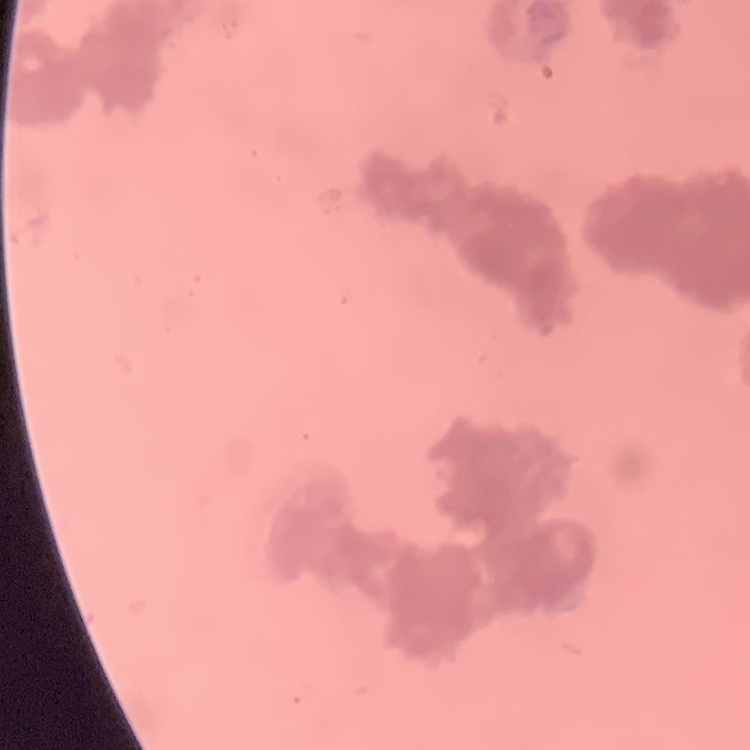

Summary:
  - Erythrocyte morphology: rouleaux formation
  - Stain: Field's or Giemsa
  - Preparation: thin blood film
  - Image type: square crop of a larger photomicrograph